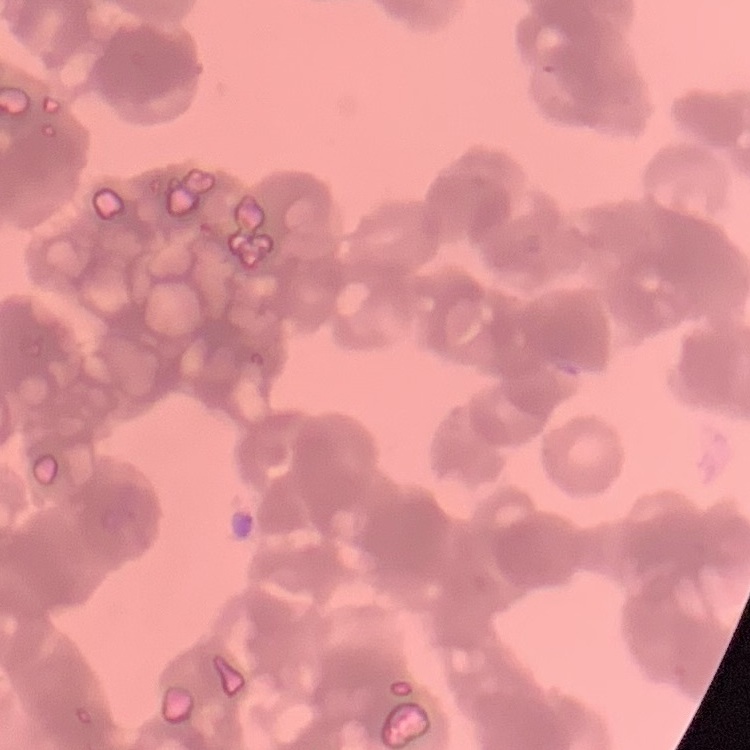
The red blood cells exhibit rouleaux formation. Field's or Giemsa stain. Thin peripheral smear. Square crop of a larger photomicrograph.